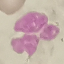
Summary:
  - Result: no malaria parasites detected
  - Stain: Giemsa
  - Preparation: thin blood film
  - Capture: smartphone camera at the microscope eyepiece
  - Image type: automatically extracted cell patch, resized to 64 × 64 pixels